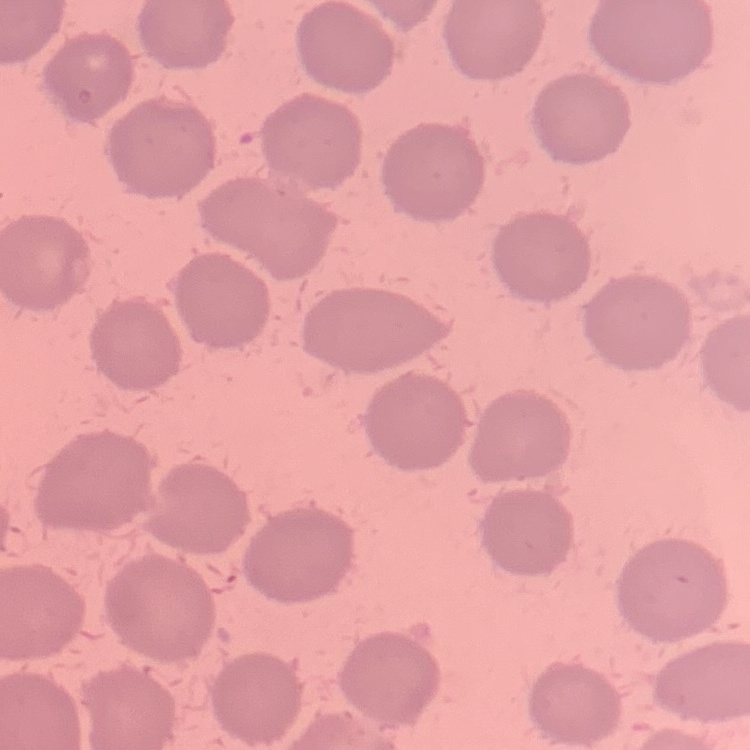
erythrocyte morphology = no rouleaux formation
stain = Field's or Giemsa
image type = one tile cut from a larger photomicrograph
preparation = thin blood film